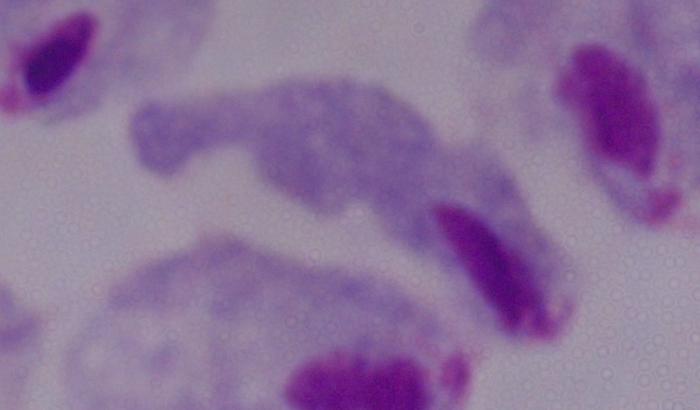 1000x magnification. A trichomonad is seen. Micrograph.